Classify the preparation.
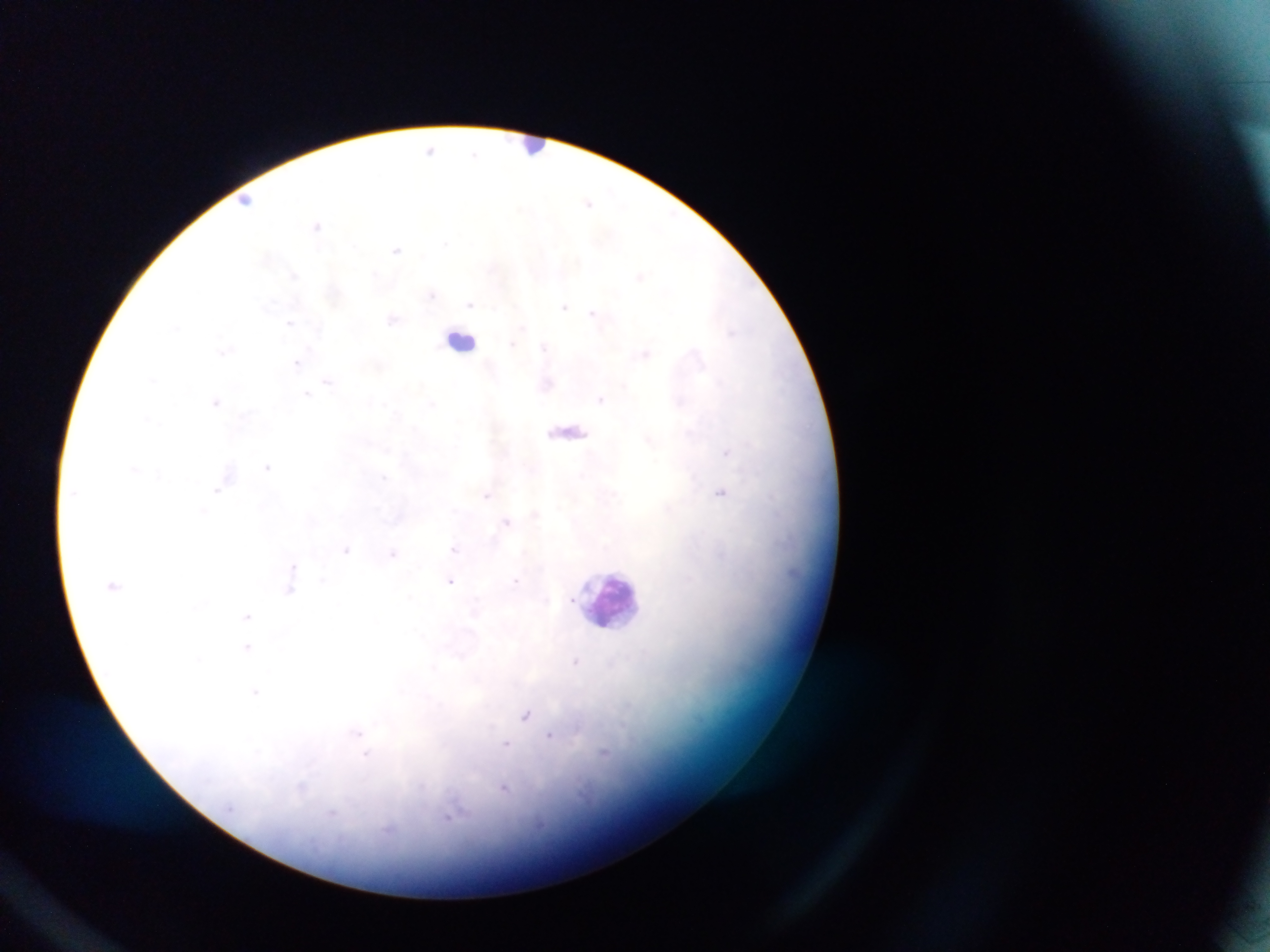
Thick blood smear.

Approximate centers as {x, y} in pixels.
Summary:
  - Malaria parasite locations: {429, 149}, {475, 155}, {248, 201}, {588, 203}, {318, 225}, {445, 243}, {397, 249}, {293, 275}, {640, 276}, {431, 295}, {470, 303}, {564, 307}, {594, 313}, {392, 319}, {289, 323}, {512, 344}, {544, 346}, {225, 351}, {645, 353}, {297, 363}, {328, 382}, {307, 393}, {600, 399}, {216, 401}, {726, 451}, {268, 466}, {134, 469}, {218, 490}, {720, 492}, {487, 495}, {203, 512}, {506, 521}, {454, 548}, {347, 549}, {393, 553}, {293, 566}, {323, 580}, {451, 580}, {516, 581}, {289, 591}, {573, 601}, {247, 616}, {247, 646}, {575, 661}, {255, 692}, {526, 715}, {358, 732}, {550, 735}, {506, 744}, {365, 755}, {302, 789}, {504, 789}, {453, 813}, {332, 814}
  - Leukocyte locations: {533, 147}, {461, 340}, {609, 600}
  - Image size: 1270×952 pixels
  - Capture: mobile-phone photograph through a microscope
  - Field of view: single
  - Country: Ghana